Point out every Plasmodium parasite and every leukocyte.
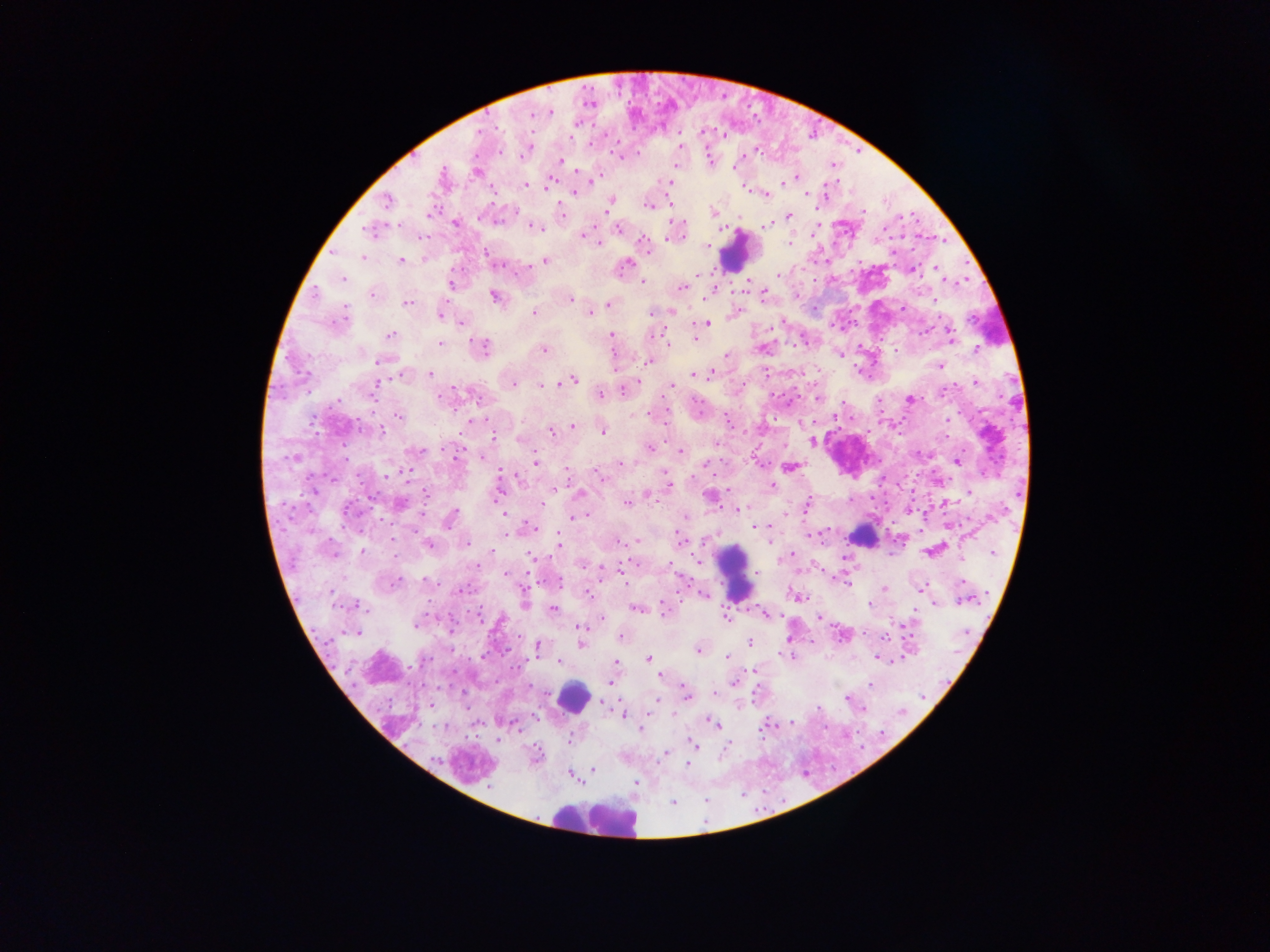
Approximate centers as x y in pixels.
Plasmodium parasites: 587 103; 550 111; 534 114; 576 124; 706 132; 749 149; 710 158; 560 161; 476 171; 578 171; 798 177; 554 181; 593 181; 668 183; 784 185; 527 186; 802 192; 573 194; 826 194; 804 195; 764 196; 670 201; 385 203; 609 205; 650 205; 608 211; 714 212; 429 215; 788 216; 455 222; 683 224; 767 224; 400 225; 526 225; 535 227; 540 227; 619 227; 368 228; 581 234; 422 236; 669 239; 644 242; 599 243; 790 243; 706 245; 362 257; 629 258; 545 260; 401 261; 625 263; 929 268; 914 269; 780 274; 343 280; 644 281; 448 286; 718 288; 681 289; 741 289; 764 294; 491 297; 571 297; 405 304; 608 305; 902 310; 534 313; 590 313; 440 314; 709 322; 460 324; 950 326; 926 330; 659 334; 952 334; 390 335; 611 336; 695 339; 665 342; 440 345; 482 346; 977 348; 543 350; 726 355; 650 361; 377 362; 941 366; 713 368; 711 372; 430 374; 691 376; 400 377; 574 378; 640 378; 975 383; 548 384; 377 385; 513 385; 455 386; 540 386; 669 386; 624 388; 600 393; 939 394; 442 395; 341 400; 910 400; 336 401; 666 407; 400 415; 476 419; 727 419; 351 421; 573 424; 381 430; 550 432; 604 432; 495 437; 813 441; 649 447; 421 450; 681 450; 458 452; 454 457; 292 459; 957 462; 535 463; 705 464; 759 464; 622 465; 793 467; 567 471; 407 472; 664 472; 501 475; 386 477; 773 487; 668 488; 424 492; 577 492; 972 492; 646 494; 426 496; 495 496; 651 496; 712 496; 806 500; 399 503; 626 503; 542 504; 805 509; 736 510; 504 513; 684 518; 573 519; 448 521; 768 526; 755 527; 534 528; 811 533; 678 538; 817 538; 392 539; 636 541; 466 543; 429 544; 771 544; 560 545; 335 550; 360 550; 929 552; 992 554; 844 557; 696 559; 670 564; 478 565; 600 569; 752 573; 505 574; 623 578; 398 581; 424 581; 961 581; 847 583; 922 587; 925 588; 461 589; 885 590; 330 594; 590 594; 704 594; 799 598; 961 601; 524 603; 358 604; 870 606; 635 607; 663 607; 553 608; 365 609; 763 613; 479 614; 726 615; 768 615; 819 618; 900 622; 578 623; 417 625; 448 625; 575 628; 360 630; 355 632; 884 638; 748 642; 580 645; 536 646; 698 649; 726 656; 646 658; 876 659; 558 662; 896 662; 615 663; 661 676; 735 682; 608 683; 868 687; 716 694; 686 697; 604 706; 652 706; 672 714; 533 716; 707 718; 713 724; 513 728; 639 728; 759 731; 496 742; 569 742; 693 744; 727 744; 667 753; 686 766; 591 769; 567 775.
Leukocytes: 734 248; 861 533; 737 569; 571 698; 598 823.

One field of view. Thick blood film. Image is 1270×952 pixels. Collected in Ghana. Photographed through a microscope with a mobile-phone camera.